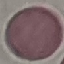
malaria_status: uninfected
preparation: thin smear
stain: Giemsa
image_type: automatically extracted cell patch, resized to 64 × 64 pixels
capture: smartphone through the microscope eyepiece